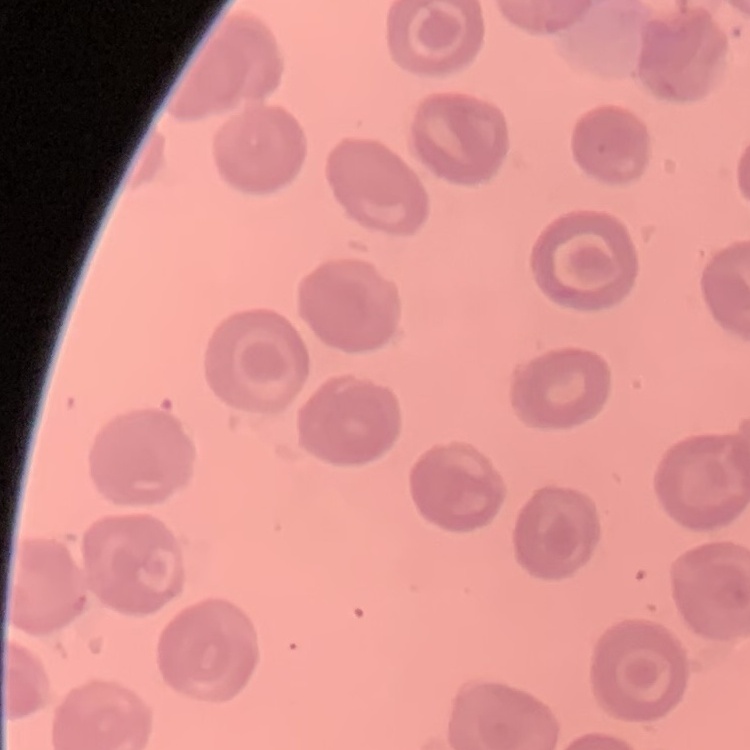

The red blood cells show no rouleaux formation. One tile cut from a larger photomicrograph. Stained with either Field's or Giemsa. Thin peripheral smear.